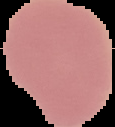
Summary:
  - Image type: segmented cell region with the area outside set to black
  - Preparation: thin blood film
  - Malaria status: uninfected
  - Image size: 115×127 pixels